Comment on the morphology of the red blood cells.
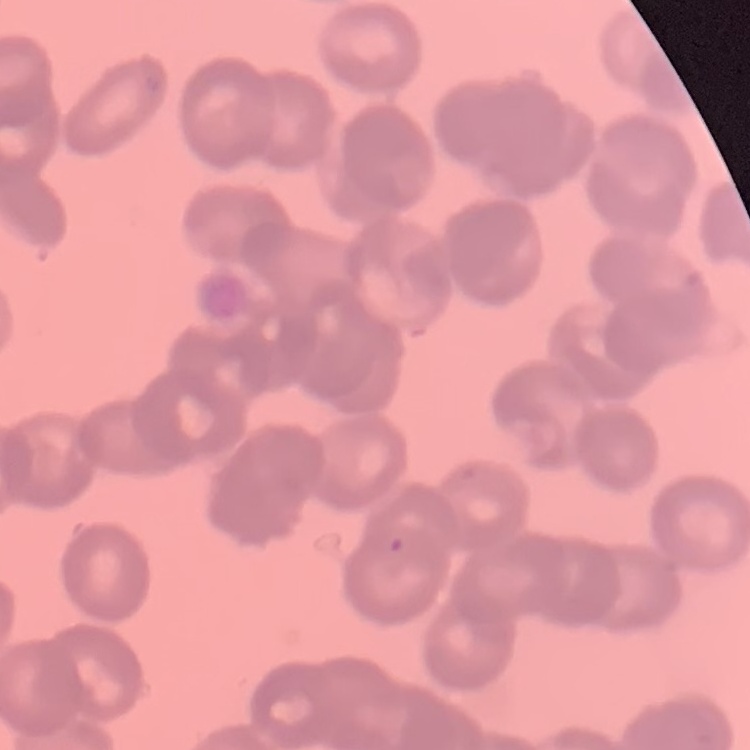

Rouleaux formation.

Summary:
  - Preparation: thin blood smear
  - Image type: one tile cut from a larger photomicrograph
  - Stain: Field's or Giemsa